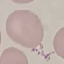 Malaria status: uninfected. Cell patch, automatically extracted from a larger field of view and resized to 64 × 64 pixels. Giemsa-stained preparation. Thin blood smear. Photographed with a smartphone camera at the microscope eyepiece.